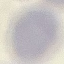
Result: no malaria parasites detected. Acquired by smartphone through the microscope eyepiece. Giemsa stain. Automatically extracted cell patch, resized to 64 × 64 pixels. Thin smear of blood.